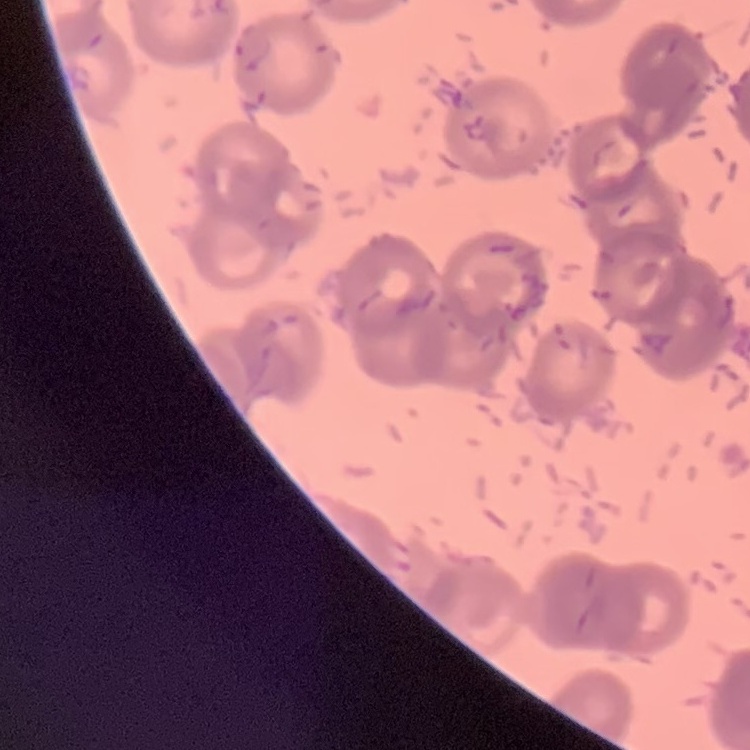

erythrocyte morphology = rouleaux formation
preparation = thin peripheral smear
stain = Field's or Giemsa
image type = square crop of a larger photomicrograph